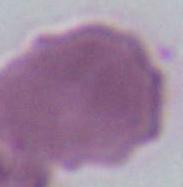

A red blood cell is seen. Micrograph. Captured at 1000x magnification.